Classify this cell by malaria status.
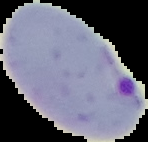

Parasitized.

image type = segmented cell region on a black background
image size = 148×142 pixels
preparation = thin blood smear